State which parasite is depicted.
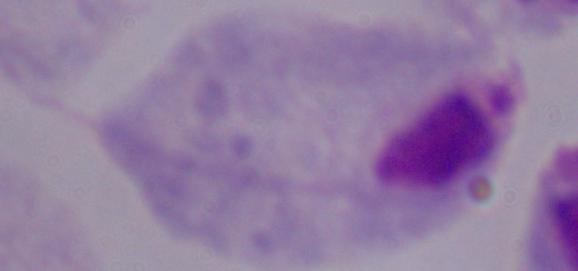

A trichomonad.

modality = photomicrograph
magnification = 1000x